State which parasite is depicted.
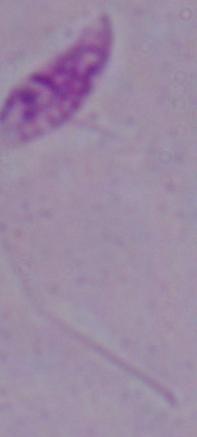
This is Leishmania.

1000x magnification. Micrograph.